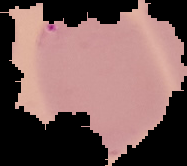

Summary:
  - Image type: segmented cell region on a black background
  - Image size: 187×166 pixels
  - Preparation: thin blood film
  - Result: Plasmodium parasites detected